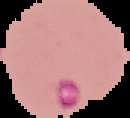
From a thin blood film. Image is 130×118 pixels. Malaria status: parasitized. Segmented cell region on a black background.